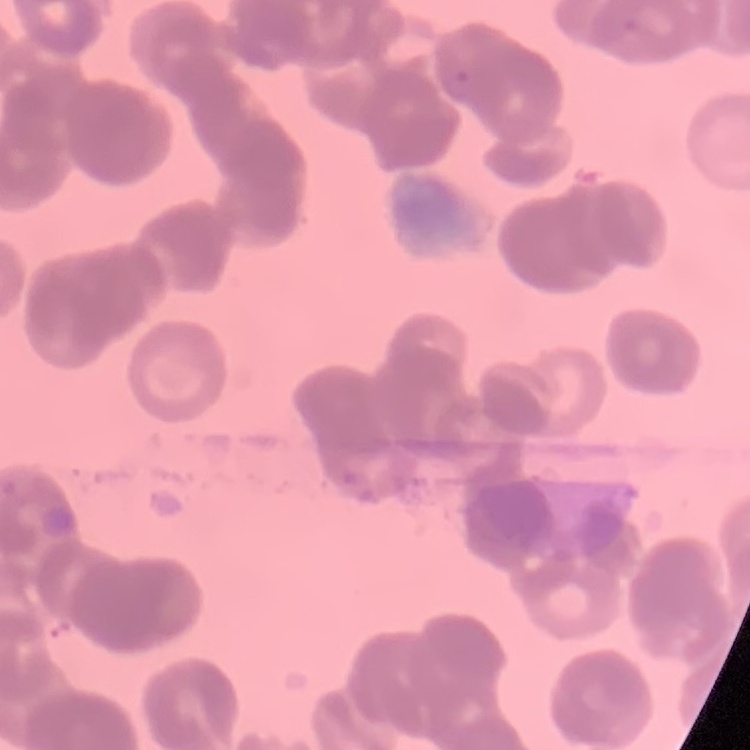
The red blood cells exhibit rouleaux formation. Thin blood film. One tile cut from a larger photomicrograph. Stained with either Field's or Giemsa.